Give the position of every leukocyte visible.
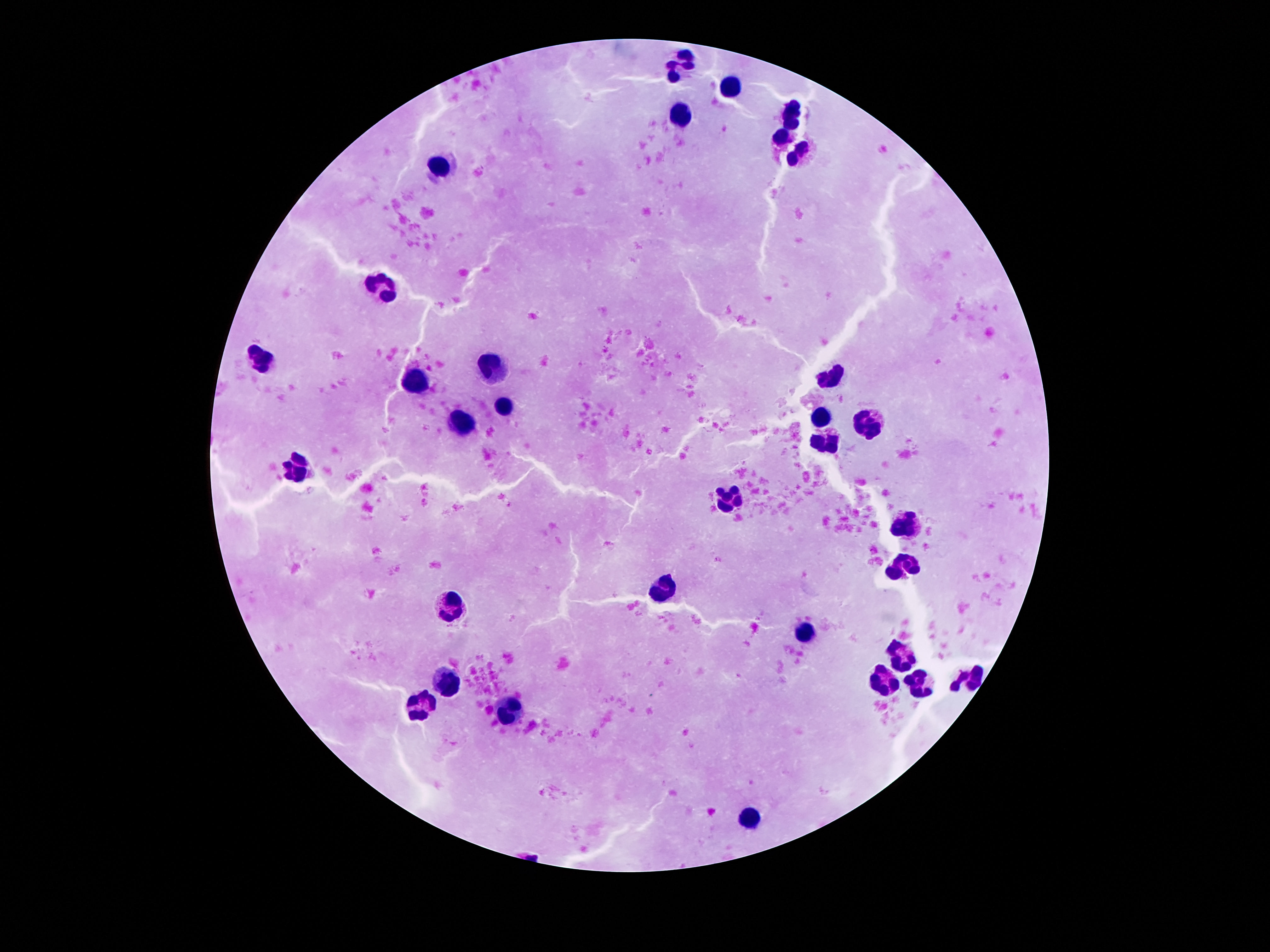

Approximate centers as (x, y) in pixels.
Leukocytes: (682, 64), (730, 87), (682, 115), (793, 116), (790, 146), (443, 163), (385, 285), (263, 358), (493, 370), (832, 375), (418, 383), (504, 402), (825, 413), (464, 420), (869, 425), (825, 444), (298, 466), (731, 496), (907, 529), (907, 566), (659, 589), (454, 608), (808, 632), (903, 656), (972, 679), (884, 681), (447, 683), (922, 686), (424, 707), (506, 709), (750, 819).

One field from this slide. Patient malaria status: not infected. Thick blood smear. Smartphone photograph taken through the microscope eyepiece. Giemsa-stained preparation. Image is 1270×952 pixels. 100x magnification.